Describe the morphology of the red blood cells.
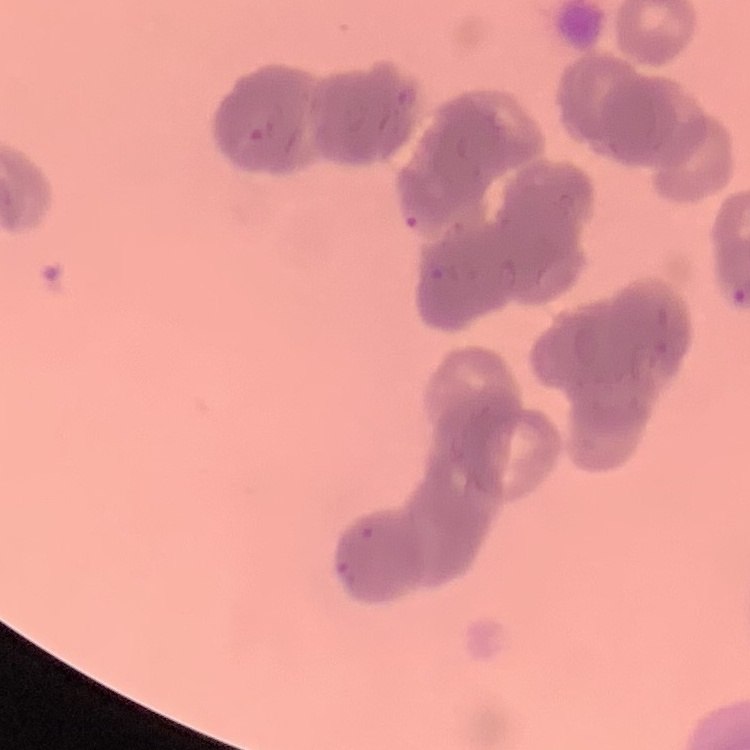

They show rouleaux formation.

Summary:
  - Stain: Field's or Giemsa
  - Image type: square crop of a larger photomicrograph
  - Preparation: thin blood film